Assess the morphology of the red blood cells.
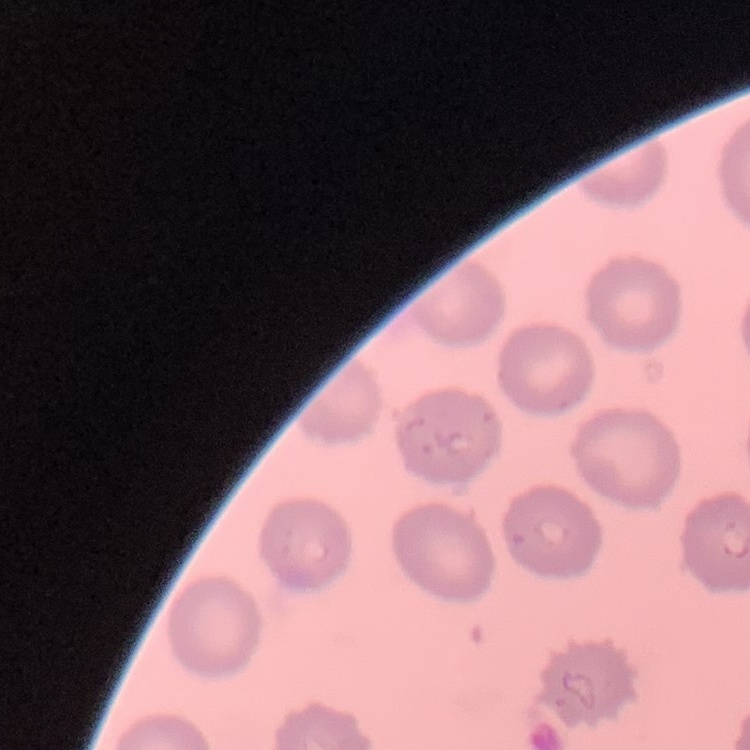
They show no rouleaux formation.

Field's or Giemsa stain. Thin blood smear. Square crop of a larger photomicrograph.